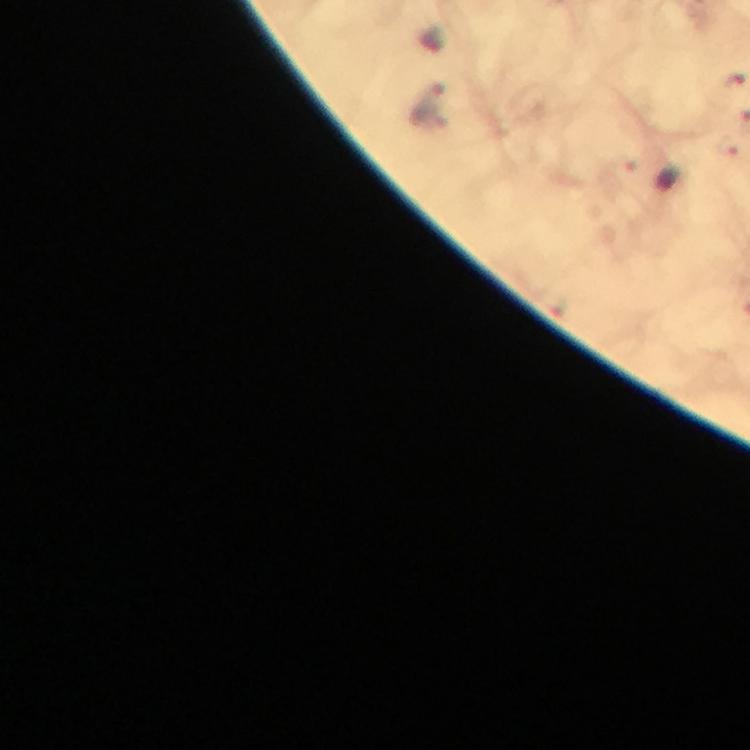

magnification: 100x
stain: Giemsa
cropped_from: one field of view
context: from a malaria diagnostic workup
plasmodium_parasite_locations: 'approximate centers as [x, y] in pixels: [734, 76], [427, 104], [727, 145]'
preparation: thick smear
image_size: 750×750 pixels
immersion_oil: used
capture: smartphone camera through the microscope